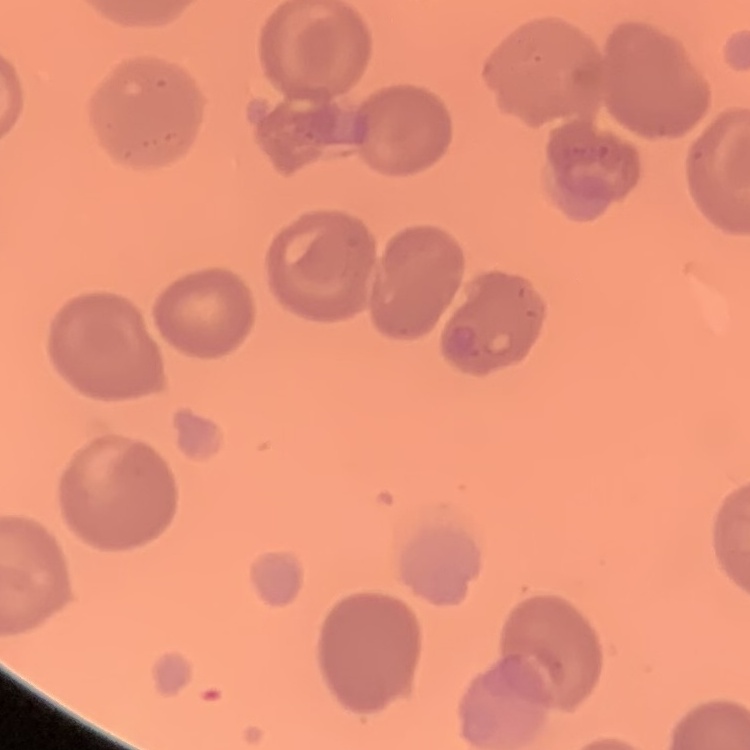
red blood cell morphology = no rouleaux formation
image type = one tile cut from a larger photomicrograph
preparation = thin blood film
stain = Field's or Giemsa